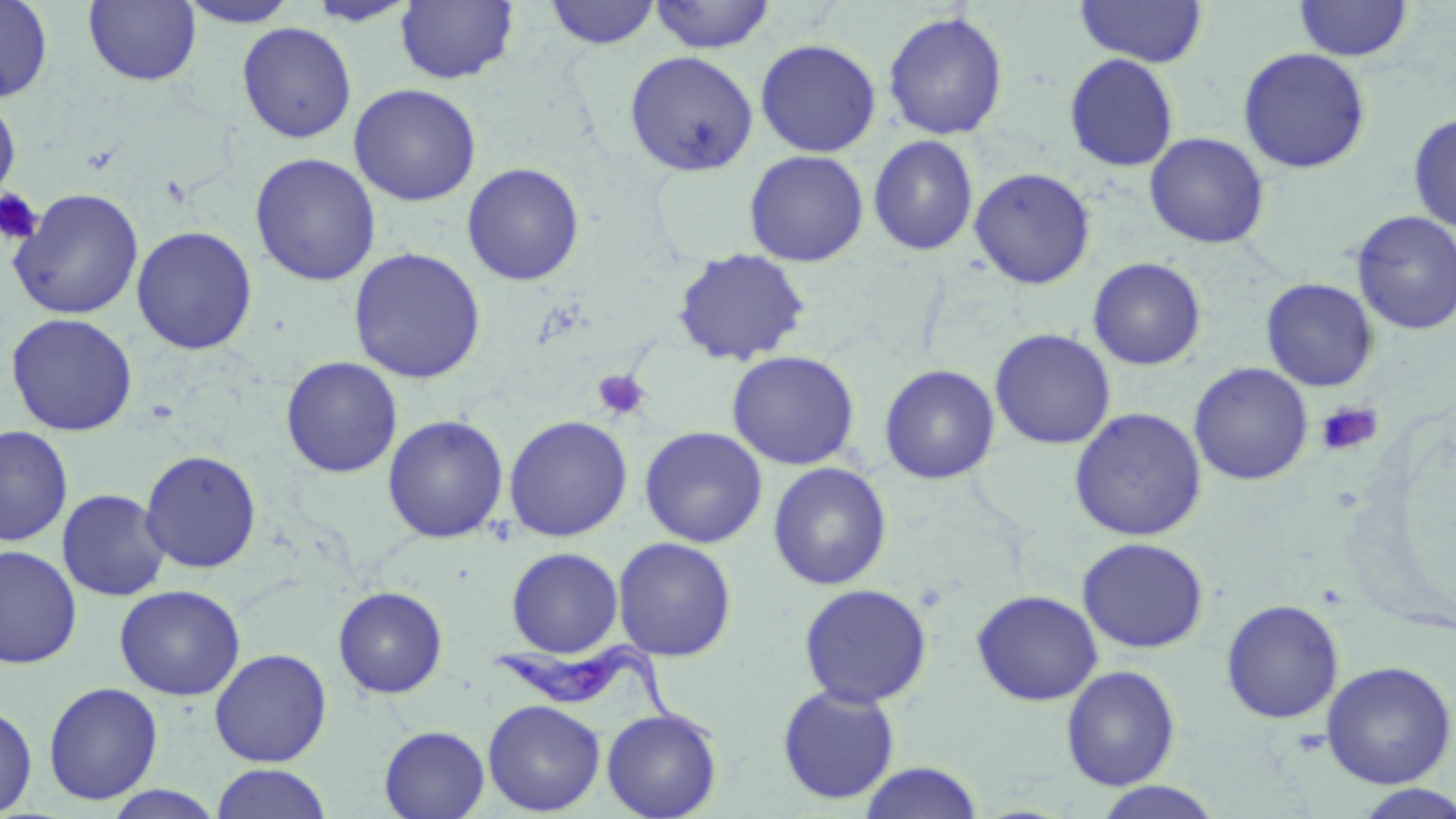

{
  "slide_level_diagnosis": "Trypanosoma brucei",
  "magnification": "1000x",
  "field_of_view": "one of a larger specimen",
  "stain": "May-Grünwald-Giemsa",
  "trypanosoma_brucei_locations": "approximate bounding boxes as (x1, y1, x2, y2) in pixels: (492, 639, 718, 746)",
  "image_size": "1456×819 pixels",
  "preparation": "thin blood smear",
  "uninfected_red_blood_cell_locations": "approximate bounding boxes as (x1, y1, x2, y2) in pixels: (0, 0, 54, 103), (174, 0, 302, 28), (396, 0, 519, 85), (543, 0, 662, 49), (648, 0, 777, 54), (1074, 0, 1208, 67), (1294, 0, 1413, 62), (83, 1, 202, 86), (303, 1, 421, 27), (882, 10, 1009, 141), (237, 22, 357, 144), (755, 38, 882, 158), (1237, 47, 1372, 174), (624, 50, 759, 177), (1064, 53, 1179, 172), (348, 83, 482, 206), (0, 91, 21, 207), (1407, 113, 1456, 232), (1144, 133, 1270, 249), (868, 135, 979, 256), (743, 150, 869, 267), (249, 153, 381, 286), (461, 162, 585, 286), (969, 167, 1096, 290), (8, 188, 144, 320), (1351, 211, 1456, 335), (131, 225, 258, 355), (348, 247, 486, 383), (672, 248, 811, 366), (1087, 257, 1207, 371), (1261, 278, 1378, 392), (6, 313, 138, 436), (989, 328, 1116, 450), (726, 350, 861, 470), (281, 356, 403, 478), (1189, 362, 1313, 485), (879, 364, 1000, 485), (1069, 407, 1207, 541), (382, 414, 509, 544), (503, 415, 633, 542), (1, 425, 74, 547), (639, 426, 768, 548), (140, 449, 262, 573), (768, 462, 892, 590), (57, 488, 171, 601), (612, 537, 738, 662), (1077, 537, 1210, 654), (0, 544, 82, 669), (506, 547, 624, 658), (798, 583, 933, 708), (114, 584, 246, 701), (333, 586, 448, 699), (971, 589, 1103, 707), (1220, 599, 1344, 724), (209, 648, 332, 767), (1320, 661, 1456, 789), (1061, 665, 1181, 791), (42, 681, 163, 805), (776, 684, 901, 806), (483, 699, 605, 815), (0, 702, 37, 818), (601, 708, 723, 819), (379, 725, 490, 818), (858, 761, 985, 819), (211, 763, 333, 819), (1092, 781, 1226, 818), (1350, 784, 1456, 818), (98, 785, 228, 818)",
  "platelet_locations": "approximate bounding boxes as (x1, y1, x2, y2) in pixels: (0, 188, 44, 246), (592, 369, 651, 421), (1315, 400, 1383, 456)",
  "modality": "light microscopy"
}